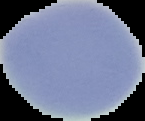
From a thin blood film. The area outside the segmented cell region is set to black. Malaria status: uninfected. Image is 145×121 pixels.